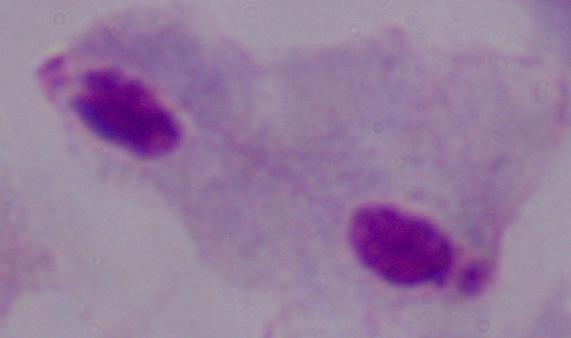
magnification = 1000x
identification = trichomonad
modality = micrograph